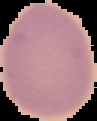

Image is 97×121 pixels. Result: no Plasmodium parasites detected. The area outside the segmented cell region is set to black. From a thin blood smear.